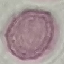
Summary:
  - Malaria status: uninfected
  - Stain: Giemsa
  - Image type: automatically extracted cell patch, resized to 64 × 64 pixels
  - Preparation: thin blood film
  - Capture: smartphone camera at the microscope eyepiece